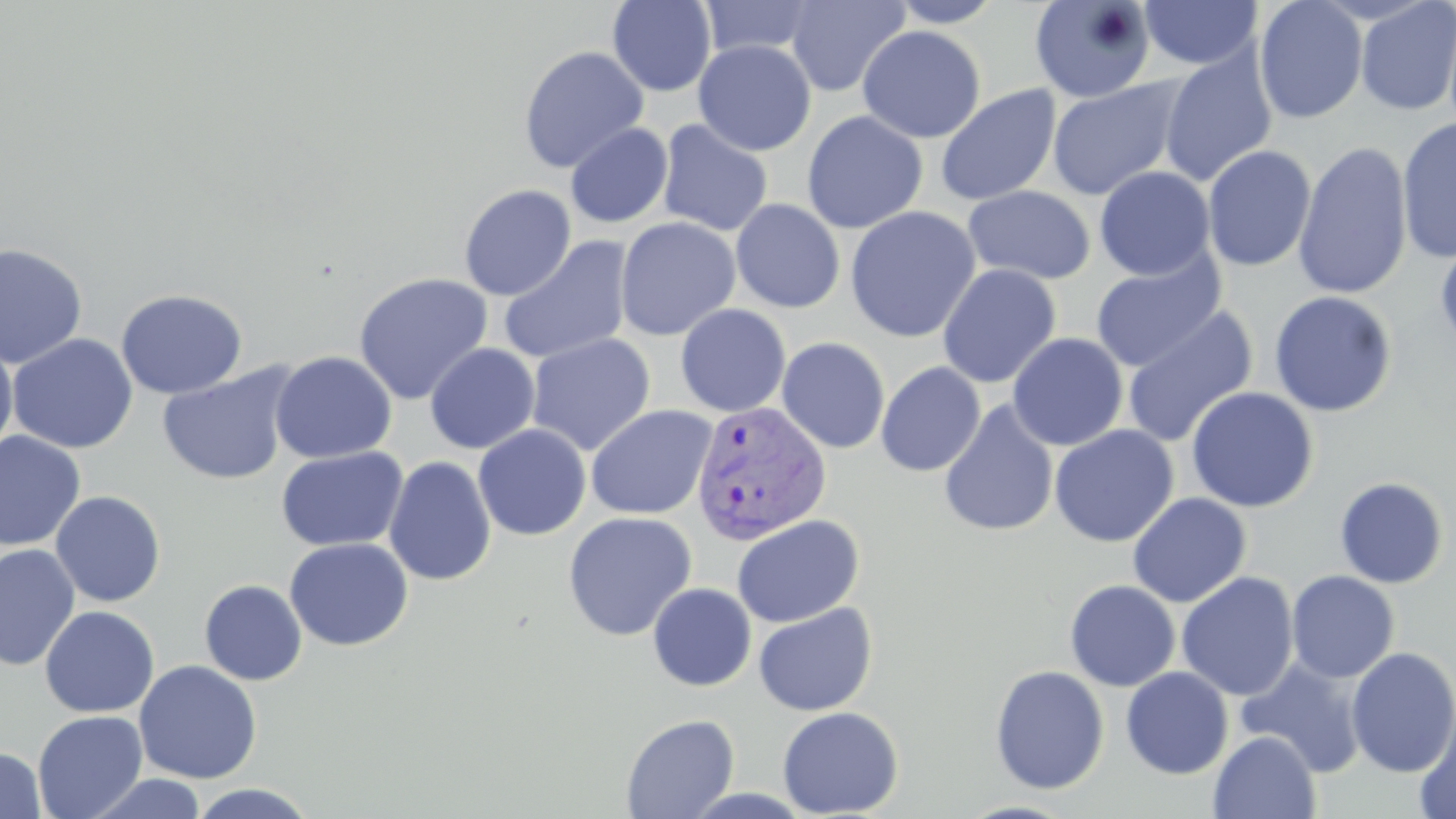
Summary:
  - Coordinate format: approximate bounding boxes as [x1, y1, x2, y2] in pixels
  - Uninfected red blood cell locations: [785, 0, 910, 97], [886, 0, 1006, 28], [1029, 0, 1158, 104], [1138, 0, 1263, 70], [1254, 0, 1368, 124], [607, 1, 717, 97], [698, 1, 821, 58], [1354, 1, 1456, 116], [857, 25, 986, 143], [693, 40, 816, 156], [518, 45, 649, 174], [1158, 48, 1278, 188], [1047, 77, 1184, 200], [935, 84, 1061, 206], [802, 111, 928, 234], [1397, 117, 1456, 264], [656, 119, 773, 237], [565, 123, 673, 228], [1293, 140, 1413, 301], [1202, 144, 1316, 272], [1094, 166, 1215, 281], [458, 184, 576, 300], [962, 186, 1096, 285], [731, 198, 845, 313], [845, 205, 981, 343], [614, 217, 741, 341], [499, 236, 634, 365], [1434, 237, 1456, 356], [0, 242, 89, 370], [1090, 252, 1226, 372], [937, 264, 1061, 389], [353, 272, 493, 405], [115, 288, 248, 399], [1268, 290, 1397, 417], [675, 304, 791, 417], [1122, 304, 1258, 448], [7, 333, 138, 454], [525, 333, 656, 456], [1007, 333, 1129, 451], [776, 337, 890, 454], [0, 338, 18, 463], [425, 344, 540, 454], [270, 351, 397, 463], [876, 361, 986, 477], [157, 364, 298, 486], [1185, 386, 1319, 513], [938, 400, 1060, 538], [586, 404, 718, 520], [473, 424, 592, 541], [1049, 425, 1178, 546], [0, 430, 86, 552], [276, 447, 409, 552], [384, 456, 497, 587], [1334, 476, 1450, 589], [50, 491, 166, 607], [1127, 492, 1251, 607], [562, 511, 697, 641], [731, 514, 865, 628], [284, 538, 412, 651], [0, 543, 81, 671], [1286, 570, 1400, 683], [1176, 571, 1299, 701], [199, 579, 307, 686], [1064, 580, 1181, 691], [647, 582, 757, 691], [753, 602, 877, 716], [39, 605, 159, 718], [1346, 647, 1456, 778], [1237, 658, 1367, 778], [134, 660, 262, 784], [989, 664, 1109, 795], [1120, 667, 1234, 779], [777, 706, 903, 818], [1414, 707, 1456, 819], [32, 710, 148, 819], [620, 713, 739, 818], [1208, 732, 1321, 819], [0, 746, 47, 819], [84, 773, 209, 818], [187, 784, 319, 819]
  - Plasmodium vivax-infected red blood cell locations: [689, 401, 833, 545]
  - Slide-level diagnosis: Plasmodium vivax
  - Image size: 1456×819 pixels
  - Magnification: 1000x
  - Modality: optical microscopy
  - Stain: May-Grünwald-Giemsa
  - Preparation: thin blood film
  - Field of view: one of a larger specimen